State the blood parasite species.
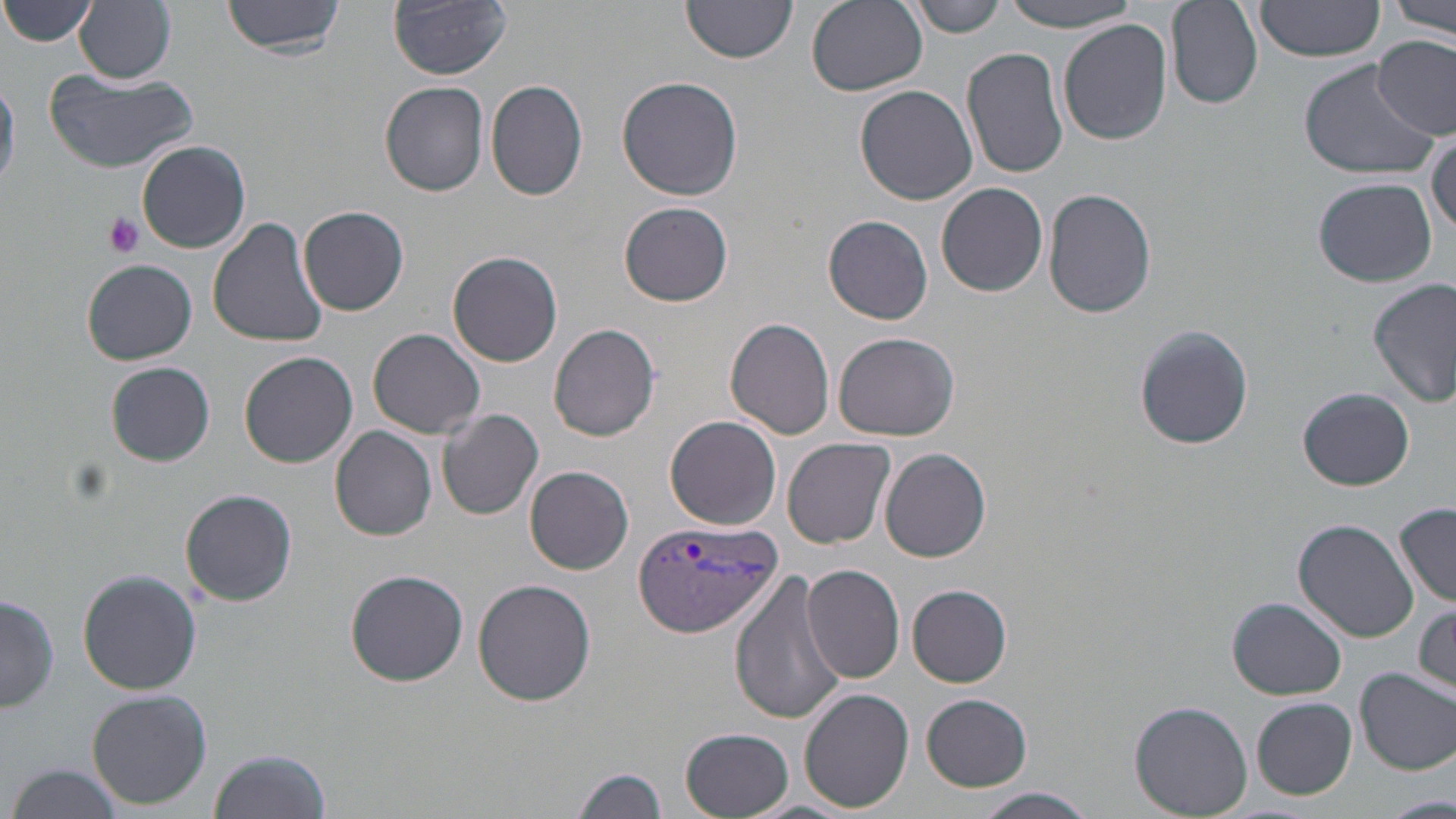

Plasmodium vivax.

uninfected red blood cell locations = approximate bounding boxes as (x1,y1)-(x2,y2) corner pairs in pixels: (2,0)-(99,48), (224,0)-(345,57), (390,0)-(513,79), (806,0)-(927,96), (912,0)-(1008,37), (1002,0)-(1145,32), (1163,0)-(1261,110), (1254,0)-(1388,67), (1387,0)-(1456,38), (75,1)-(176,84), (681,1)-(796,67), (1059,20)-(1172,145), (1373,36)-(1455,140), (962,47)-(1070,181), (1297,58)-(1438,179), (42,68)-(197,174), (617,75)-(744,201), (0,77)-(21,193), (486,80)-(590,203), (381,81)-(491,197), (855,85)-(977,205), (1427,129)-(1455,235), (137,140)-(250,253), (1313,177)-(1438,286), (936,182)-(1047,296), (1043,188)-(1156,318), (619,202)-(734,306), (298,206)-(409,316), (822,214)-(934,326), (206,216)-(329,348), (448,251)-(563,367), (83,258)-(198,365), (1368,279)-(1455,406), (724,316)-(834,440), (549,323)-(663,441), (1133,323)-(1252,451), (368,328)-(486,439), (834,330)-(960,441), (240,351)-(359,468), (107,362)-(215,466), (1297,386)-(1415,491), (438,409)-(544,520), (665,415)-(781,529), (330,427)-(438,542), (783,437)-(896,548), (882,447)-(992,564), (526,465)-(634,574), (180,488)-(298,607), (1395,504)-(1456,608), (1294,519)-(1421,642), (801,564)-(904,683), (77,569)-(203,695), (343,570)-(469,686), (730,571)-(846,725), (473,578)-(597,705), (907,585)-(1011,685), (2,592)-(59,713), (1229,597)-(1346,699), (1413,600)-(1455,697), (1355,667)-(1456,774), (801,688)-(916,811), (87,690)-(212,809), (922,693)-(1035,792), (1252,697)-(1357,799), (1130,701)-(1254,819), (680,729)-(793,818), (210,748)-(330,819), (5,762)-(124,819), (571,765)-(669,819), (970,787)-(1100,819), (1383,794)-(1453,819)
stain = May-Grünwald-Giemsa
preparation = thin blood film
image size = 1456×819 pixels
Plasmodium vivax-infected red blood cell locations = approximate bounding boxes as (x1,y1)-(x2,y2) corner pairs in pixels: (633,520)-(781,638)
field of view = one of a larger specimen
platelet locations = approximate bounding boxes as (x1,y1)-(x2,y2) corner pairs in pixels: (103,211)-(144,255)
magnification = 1000x
modality = optical microscopy